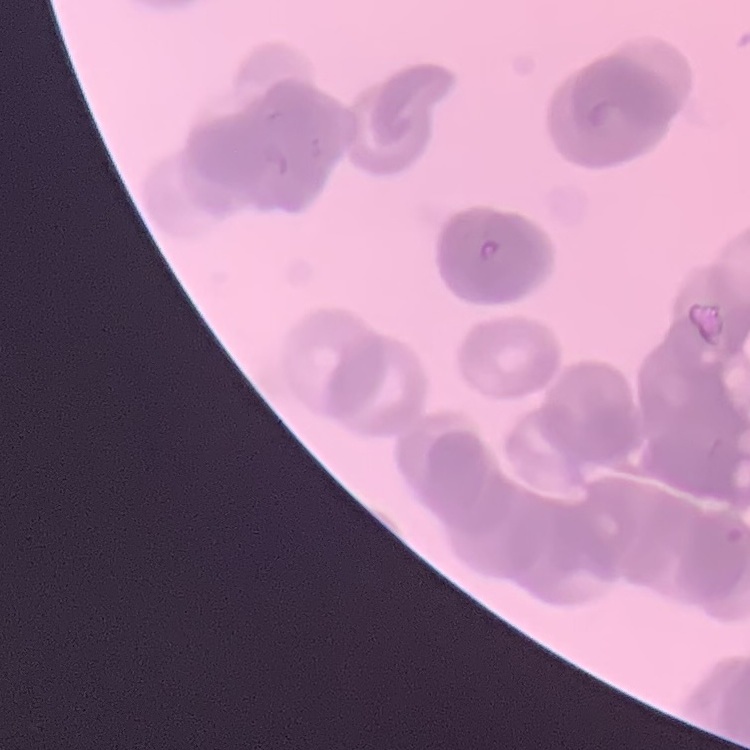
red_blood_cell_morphology: rouleaux formation
image_type: one tile cut from a larger photomicrograph
stain: Field's or Giemsa
preparation: thin blood smear